Assess this cell for malaria.
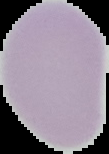
Uninfected.

Image is 109×154 pixels. From a thin blood smear. The area outside the segmented cell region is set to black.